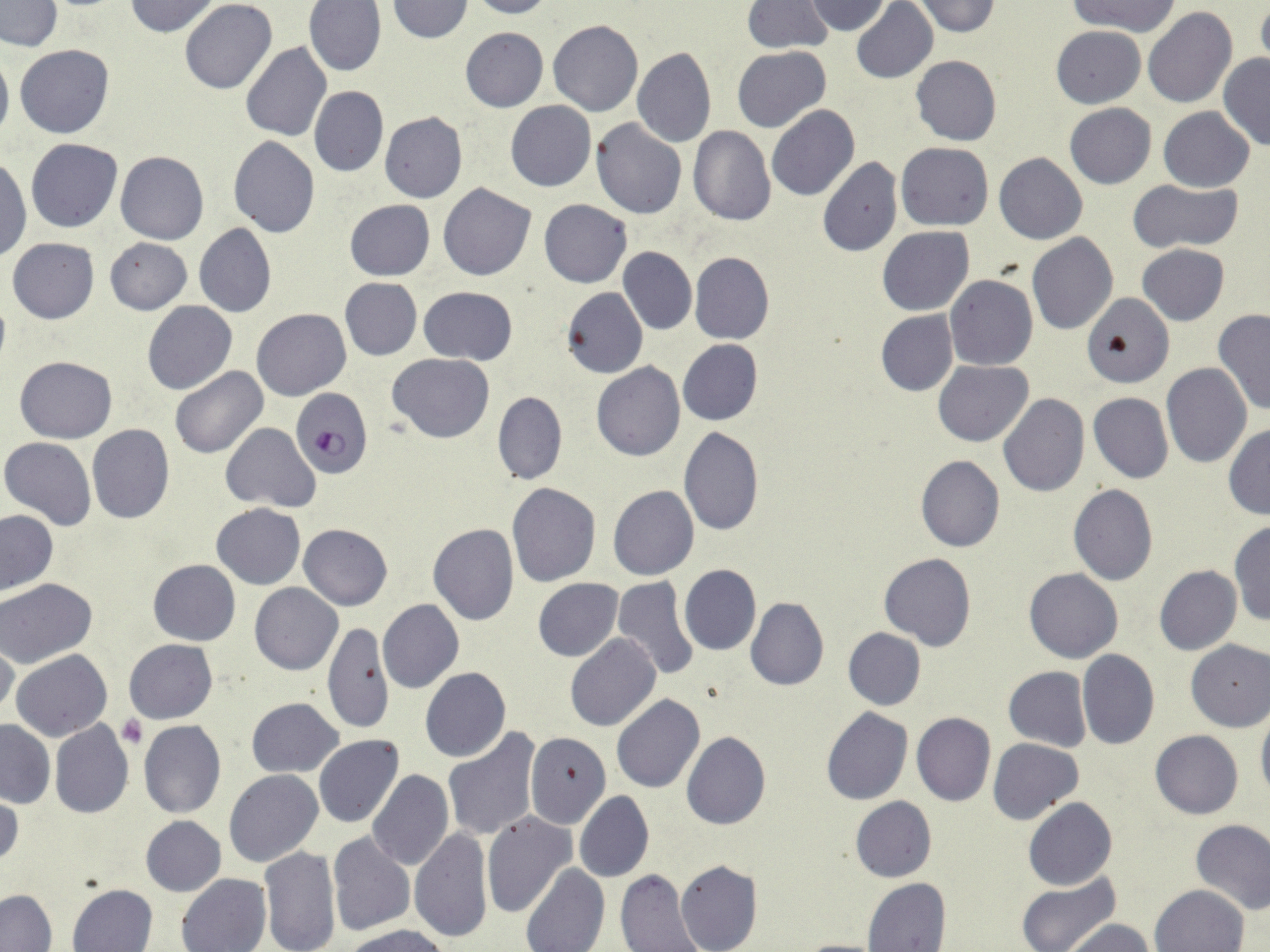

Summary:
  - Coordinate format: approximate bounding boxes as (x1, y1, x2, y2) in pixels
  - Plasmodium falciparum-infected red blood cell locations: (289, 386, 372, 478)
  - Platelet locations: (119, 715, 146, 747)
  - Uninfected red blood cell locations: (124, 0, 222, 37), (388, 0, 474, 43), (467, 0, 554, 19), (803, 0, 892, 35), (1067, 0, 1179, 37), (1, 1, 62, 51), (181, 1, 276, 94), (304, 1, 387, 76), (850, 1, 937, 84), (909, 1, 1001, 36), (740, 2, 832, 53), (1256, 5, 1270, 68), (1143, 7, 1238, 108), (548, 20, 644, 117), (1051, 26, 1145, 107), (460, 27, 548, 112), (241, 42, 333, 142), (0, 45, 13, 147), (15, 45, 115, 139), (732, 46, 831, 133), (632, 47, 716, 149), (1219, 53, 1270, 150), (911, 55, 1001, 146), (309, 85, 388, 177), (506, 101, 596, 191), (1064, 103, 1156, 188), (767, 105, 860, 201), (1159, 107, 1254, 192), (379, 112, 468, 202), (591, 119, 687, 219), (687, 126, 776, 226), (228, 137, 320, 238), (25, 139, 122, 232), (896, 142, 994, 230), (116, 150, 208, 244), (994, 152, 1087, 244), (0, 155, 31, 262), (818, 157, 902, 256), (1127, 179, 1242, 253), (439, 182, 536, 281), (539, 199, 632, 287), (344, 200, 435, 280), (194, 224, 276, 318), (878, 226, 973, 314), (1027, 232, 1118, 335), (6, 237, 99, 324), (104, 237, 192, 314), (1137, 244, 1229, 325), (618, 247, 696, 334), (689, 252, 775, 344), (945, 273, 1038, 371), (340, 278, 422, 360), (419, 286, 518, 364), (561, 288, 648, 378), (1084, 293, 1171, 387), (143, 300, 238, 395), (1212, 307, 1270, 417), (252, 308, 351, 401), (875, 310, 959, 396), (678, 339, 762, 426), (387, 354, 494, 443), (15, 356, 116, 444), (933, 360, 1032, 446), (591, 362, 685, 461), (1162, 363, 1252, 467), (170, 367, 267, 458), (493, 392, 567, 485), (1089, 393, 1174, 483), (997, 394, 1089, 498), (221, 423, 321, 511), (87, 424, 174, 524), (1225, 424, 1270, 518), (678, 426, 764, 536), (1, 437, 96, 530), (916, 455, 1005, 553), (507, 483, 600, 587), (1069, 485, 1158, 586), (608, 486, 700, 581), (211, 503, 305, 589), (1, 510, 57, 595), (1229, 520, 1270, 627), (428, 523, 518, 625), (299, 524, 393, 610), (878, 552, 976, 651), (148, 558, 240, 644), (679, 564, 761, 655), (1153, 565, 1242, 654), (1024, 568, 1124, 663), (610, 577, 700, 681), (533, 578, 623, 660), (0, 579, 98, 668), (250, 583, 342, 674), (745, 596, 829, 692), (377, 600, 464, 694), (323, 624, 392, 734), (843, 628, 925, 711), (565, 634, 660, 733), (0, 639, 19, 719), (124, 639, 218, 723), (1185, 639, 1269, 731), (11, 649, 111, 741), (1077, 650, 1159, 751), (420, 667, 510, 762), (1003, 667, 1093, 752), (611, 694, 705, 793), (247, 697, 344, 777), (821, 707, 912, 805), (1256, 710, 1270, 806), (912, 712, 996, 805), (49, 719, 134, 819), (0, 720, 54, 808), (138, 720, 225, 817), (441, 728, 540, 840), (1149, 730, 1243, 819), (524, 732, 610, 828), (682, 732, 770, 830), (314, 735, 404, 828), (988, 737, 1084, 826), (224, 770, 324, 867), (368, 770, 453, 871), (1, 790, 22, 874), (574, 790, 655, 883), (850, 795, 936, 881), (1023, 798, 1117, 891), (482, 812, 576, 917), (140, 815, 225, 897), (1190, 819, 1270, 915), (410, 828, 492, 941), (327, 832, 415, 937), (259, 847, 339, 952), (675, 858, 761, 952), (521, 863, 609, 952), (615, 869, 703, 951), (1015, 872, 1120, 952), (177, 873, 270, 952), (863, 878, 951, 952), (67, 883, 158, 952), (1151, 884, 1248, 952), (0, 890, 56, 951), (1065, 918, 1158, 952), (344, 925, 450, 952), (793, 939, 889, 952)
  - Slide-level diagnosis: Plasmodium falciparum
  - Magnification: 1000x
  - Modality: optical microscopy
  - Stain: May-Grünwald-Giemsa
  - Field of view: one of a larger specimen
  - Image size: 1270×952 pixels
  - Preparation: thin blood film